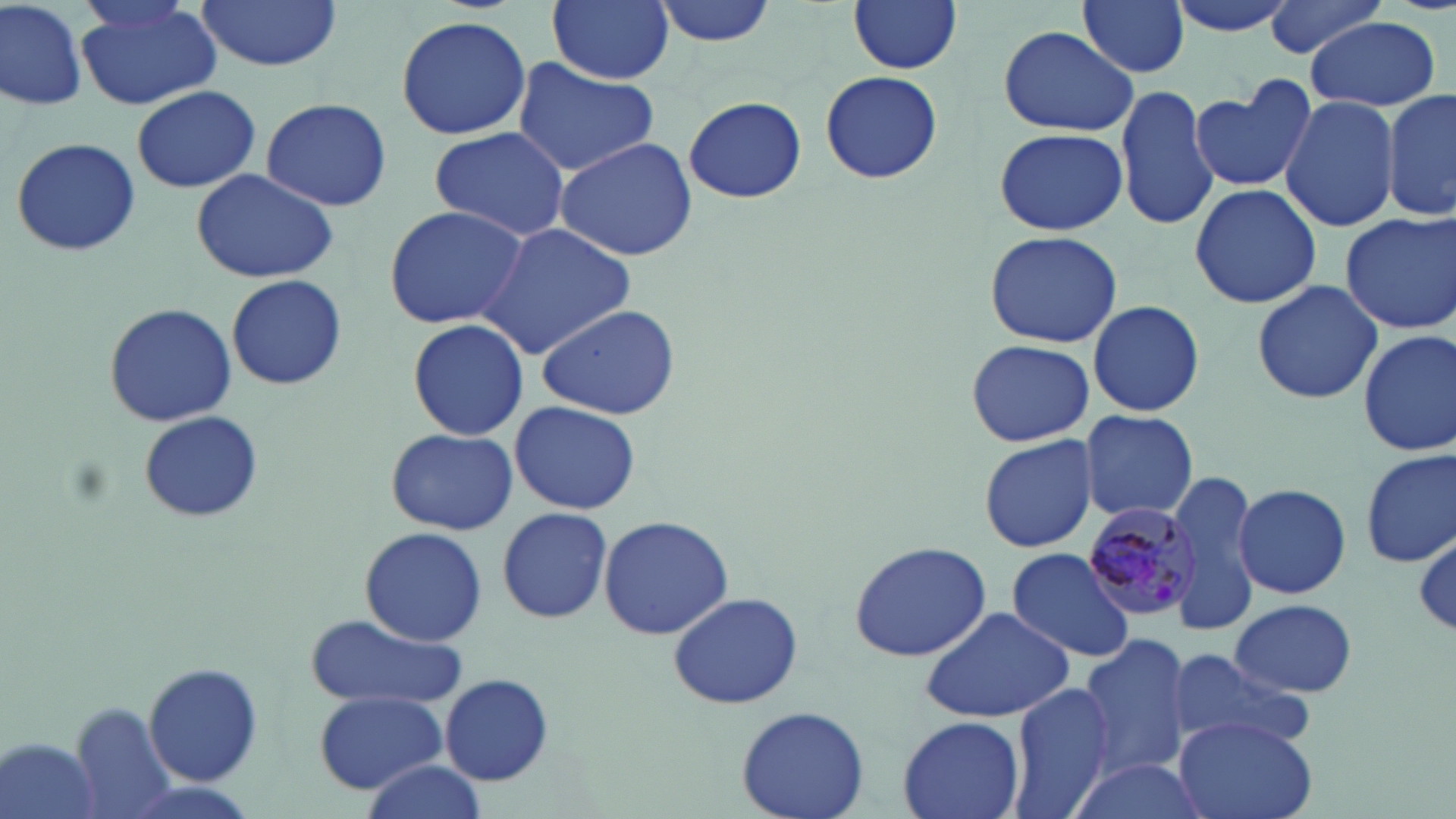

{
  "plasmodium_malariae_infected_red_blood_cell_locations": "approximate bounding boxes as named x1/y1/x2/y2 corners in pixels: (x1=1084, y1=501, x2=1203, y2=624)",
  "slide_level_diagnosis": "Plasmodium malariae",
  "stain": "May-Grünwald-Giemsa",
  "field_of_view": "one of a larger specimen",
  "uninfected_red_blood_cell_locations": "approximate bounding boxes as named x1/y1/x2/y2 corners in pixels: (x1=0, y1=0, x2=87, y2=113), (x1=193, y1=0, x2=344, y2=72), (x1=547, y1=0, x2=675, y2=83), (x1=650, y1=0, x2=778, y2=47), (x1=1078, y1=0, x2=1190, y2=78), (x1=1160, y1=0, x2=1300, y2=36), (x1=1261, y1=0, x2=1391, y2=58), (x1=848, y1=1, x2=962, y2=75), (x1=75, y1=3, x2=223, y2=111), (x1=395, y1=14, x2=532, y2=139), (x1=1306, y1=16, x2=1443, y2=112), (x1=995, y1=26, x2=1137, y2=137), (x1=513, y1=59, x2=663, y2=178), (x1=818, y1=68, x2=944, y2=186), (x1=1191, y1=77, x2=1315, y2=196), (x1=1114, y1=83, x2=1219, y2=231), (x1=132, y1=86, x2=260, y2=194), (x1=1383, y1=91, x2=1456, y2=220), (x1=1280, y1=95, x2=1399, y2=232), (x1=684, y1=96, x2=806, y2=204), (x1=258, y1=98, x2=394, y2=212), (x1=427, y1=126, x2=573, y2=242), (x1=993, y1=126, x2=1127, y2=237), (x1=555, y1=134, x2=698, y2=262), (x1=9, y1=135, x2=143, y2=260), (x1=189, y1=166, x2=338, y2=283), (x1=1190, y1=183, x2=1320, y2=310), (x1=382, y1=203, x2=532, y2=330), (x1=1337, y1=211, x2=1456, y2=334), (x1=477, y1=225, x2=637, y2=358), (x1=985, y1=230, x2=1122, y2=350), (x1=224, y1=275, x2=347, y2=392), (x1=1251, y1=280, x2=1384, y2=407), (x1=102, y1=301, x2=237, y2=427), (x1=1086, y1=301, x2=1206, y2=417), (x1=534, y1=302, x2=683, y2=420), (x1=407, y1=317, x2=528, y2=442), (x1=1356, y1=328, x2=1456, y2=460), (x1=965, y1=339, x2=1094, y2=448), (x1=509, y1=401, x2=643, y2=512), (x1=1078, y1=409, x2=1199, y2=523), (x1=138, y1=411, x2=262, y2=524), (x1=385, y1=428, x2=517, y2=535), (x1=979, y1=433, x2=1100, y2=553), (x1=1359, y1=448, x2=1455, y2=569), (x1=1165, y1=471, x2=1264, y2=631), (x1=1232, y1=482, x2=1350, y2=601), (x1=497, y1=506, x2=613, y2=624), (x1=598, y1=516, x2=736, y2=642), (x1=358, y1=525, x2=487, y2=646), (x1=1414, y1=529, x2=1456, y2=639), (x1=848, y1=539, x2=992, y2=663), (x1=1006, y1=546, x2=1137, y2=663), (x1=666, y1=591, x2=803, y2=711), (x1=1232, y1=598, x2=1356, y2=698), (x1=918, y1=606, x2=1078, y2=723), (x1=304, y1=616, x2=465, y2=714), (x1=1080, y1=635, x2=1196, y2=779), (x1=1165, y1=649, x2=1316, y2=755), (x1=143, y1=662, x2=265, y2=787), (x1=441, y1=673, x2=555, y2=786), (x1=1003, y1=680, x2=1116, y2=819), (x1=315, y1=690, x2=449, y2=794), (x1=65, y1=700, x2=177, y2=815), (x1=735, y1=705, x2=869, y2=819), (x1=897, y1=713, x2=1026, y2=819), (x1=1171, y1=716, x2=1318, y2=819), (x1=2, y1=737, x2=106, y2=819), (x1=357, y1=757, x2=486, y2=819), (x1=1062, y1=757, x2=1211, y2=819)",
  "modality": "optical microscopy",
  "image_size": "1456×819 pixels",
  "preparation": "thin blood film",
  "magnification": "1000x"
}